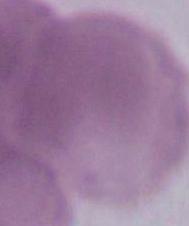

Summary:
  - Magnification: 1000x
  - Identification: erythrocyte
  - Modality: photomicrograph